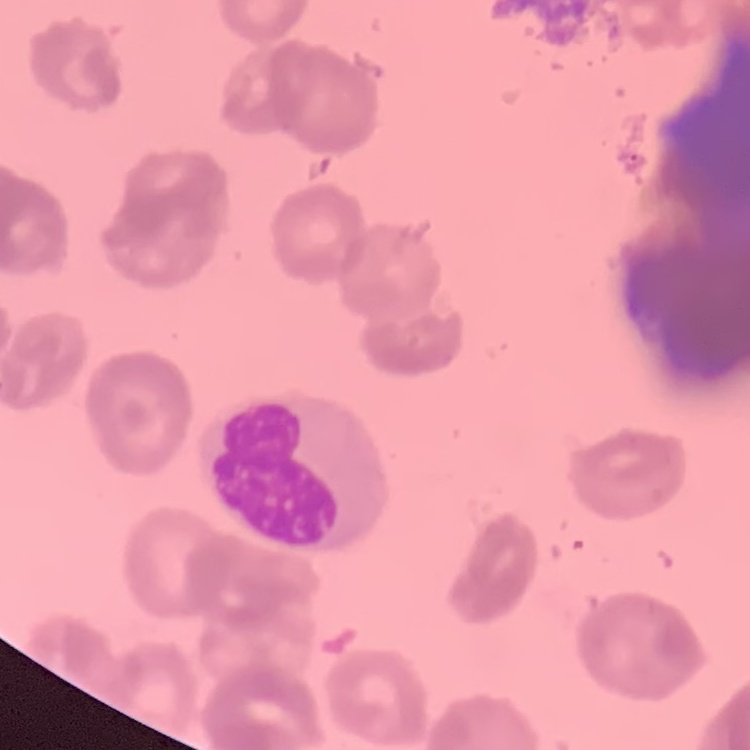 The red blood cells exhibit rouleaux formation. Field's or Giemsa stain. Thin blood smear. One tile cut from a larger photomicrograph.